Identify the parasite.
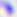
This is Toxoplasma gondii.

modality = photomicrograph
magnification = 400x